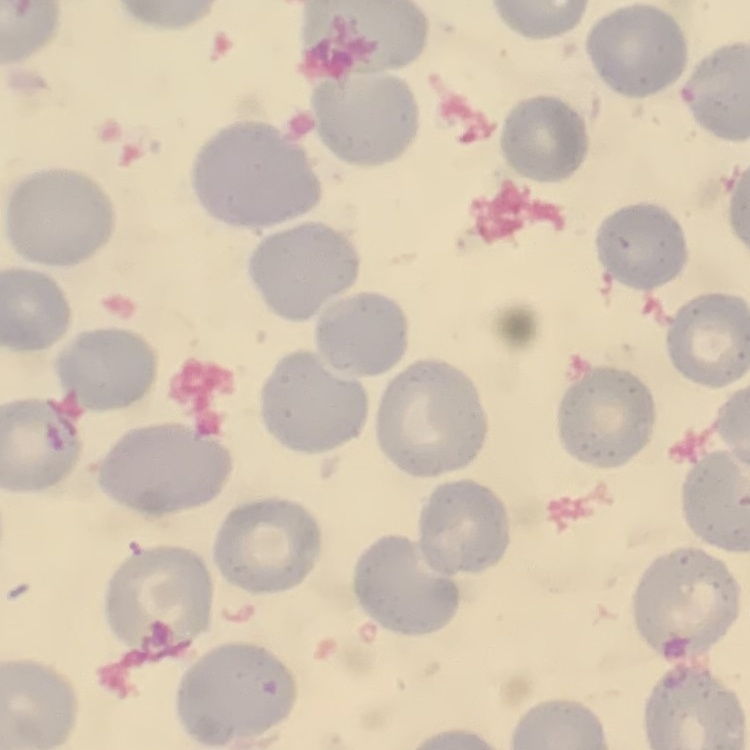 The erythrocytes exhibit no rouleaux formation. Thin blood smear. Square crop of a larger photomicrograph. Field's or Giemsa stain.